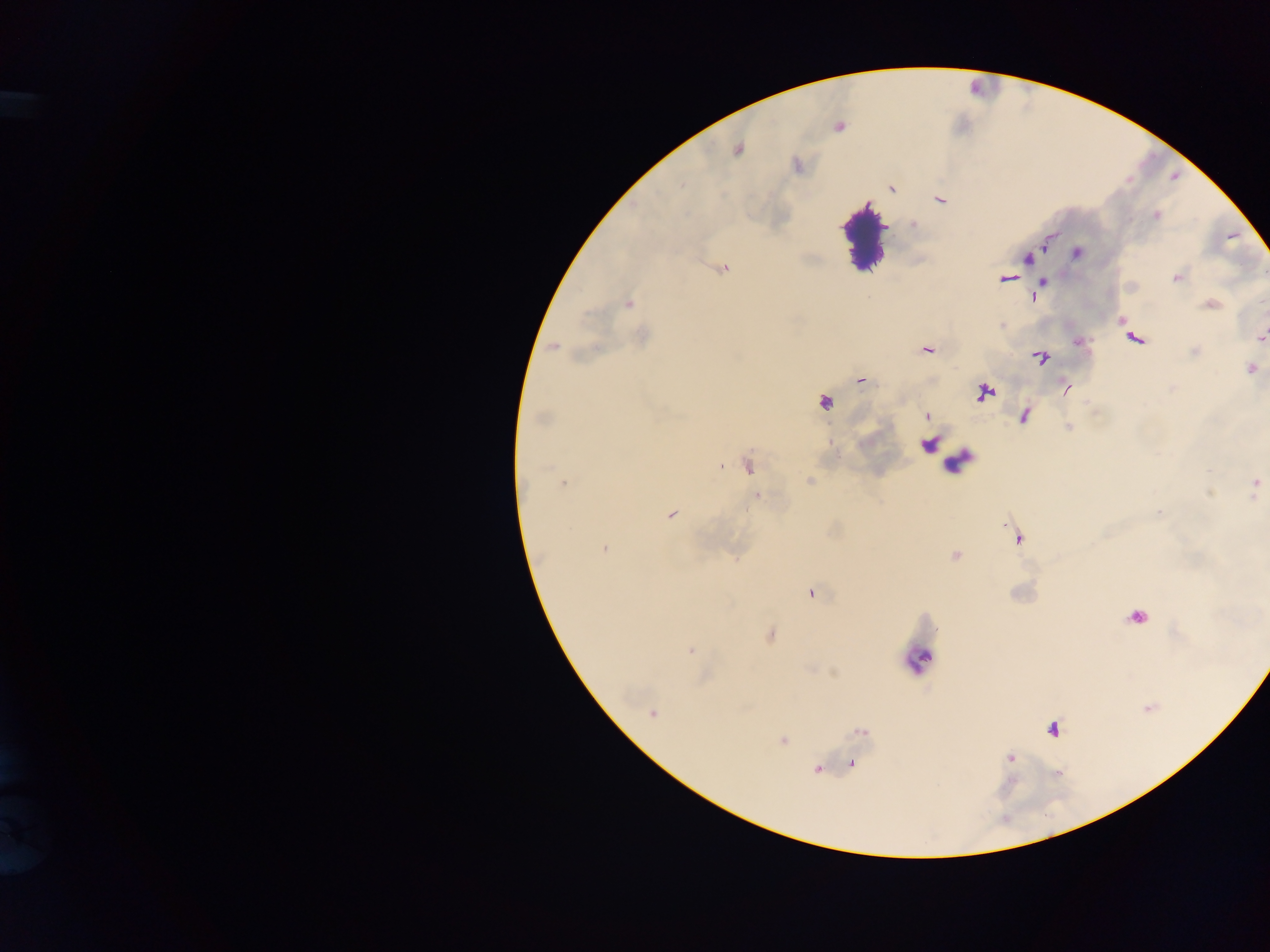

Approximate centers as (x, y) in pixels.
Summary:
  - Leukocyte locations: (863, 240), (918, 658)
  - Plasmodium parasite locations: (737, 149), (891, 189), (940, 199), (1156, 215), (1077, 252), (1027, 259), (724, 268), (1176, 278), (1006, 279), (628, 303), (1211, 304), (1261, 337), (1134, 338), (553, 347), (927, 350), (1040, 357), (1251, 369), (861, 380), (1066, 388), (985, 392), (825, 403), (926, 415), (542, 418), (1024, 423), (948, 457), (748, 467), (809, 481), (563, 484), (1255, 484), (757, 496), (670, 515), (1016, 538), (605, 548), (956, 555), (812, 594), (1137, 619), (770, 635), (690, 651), (652, 713), (1053, 729), (861, 732), (782, 740), (1011, 758), (852, 764), (817, 770)
  - Image size: 1270×952 pixels
  - Field of view: single
  - Capture: mobile-phone photograph through a microscope
  - Preparation: thick blood smear
  - Country: Ghana